Report the malaria status of this cell.
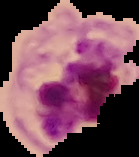

It is parasitized.

Image is 139×157 pixels. Segmented cell region on a black background. From a thin blood film.